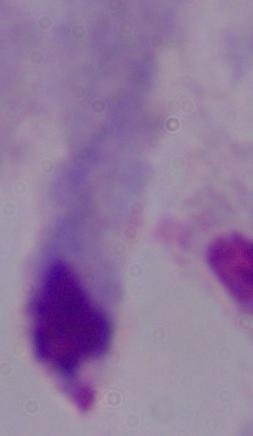
identification = trichomonad
magnification = 1000x
modality = micrograph